Name the parasite shown.
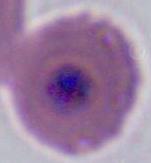
Plasmodium.

{
  "modality": "photomicrograph",
  "magnification": "400x or 1000x"
}